Assess this cell for malaria.
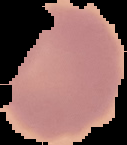

Uninfected.

Summary:
  - Preparation: thin blood smear
  - Image type: segmented cell region on a black background
  - Image size: 127×145 pixels